Report the malaria status of this cell.
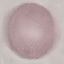

Uninfected.

Cell patch, automatically extracted from a larger field of view and resized to 64 × 64 pixels. Giemsa stain. Thin blood smear. Photographed with a smartphone camera at the microscope eyepiece.